Identify the parasite.
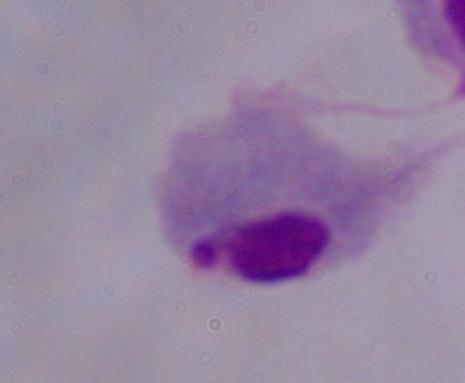

This is a trichomonad.

Micrograph. 1000x magnification.